Describe the morphology of the red blood cells.
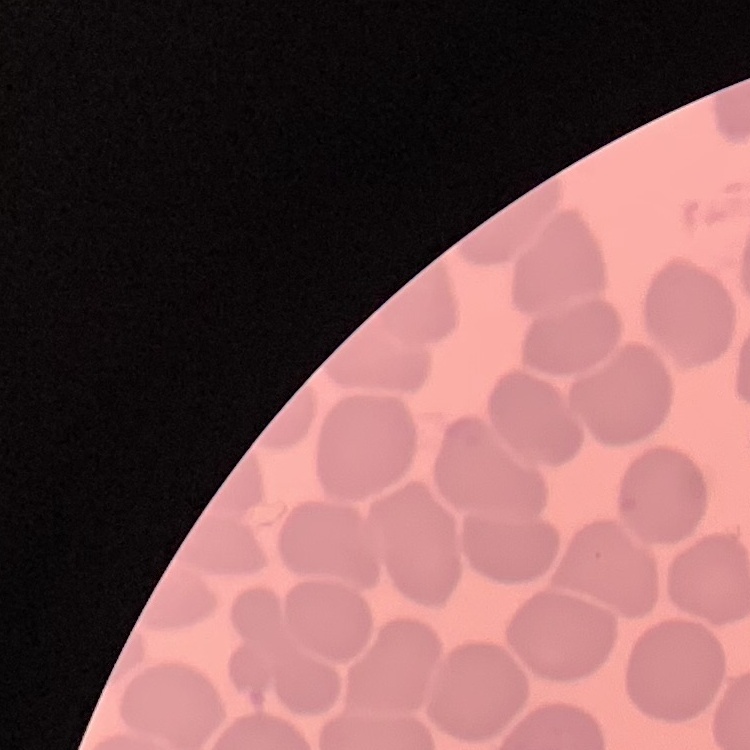
They show no rouleaux formation.

Thin peripheral smear. One tile cut from a larger photomicrograph. Field's or Giemsa stain.